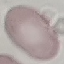

result = no malaria parasites detected
preparation = thin smear
stain = Giemsa
image type = automatically extracted cell patch, resized to 64 × 64 pixels
capture = smartphone through the microscope eyepiece